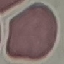
Summary:
  - Malaria status: uninfected
  - Stain: Giemsa
  - Image type: automatically extracted cell patch, resized to 64 × 64 pixels
  - Capture: smartphone through the microscope eyepiece
  - Preparation: thin blood smear